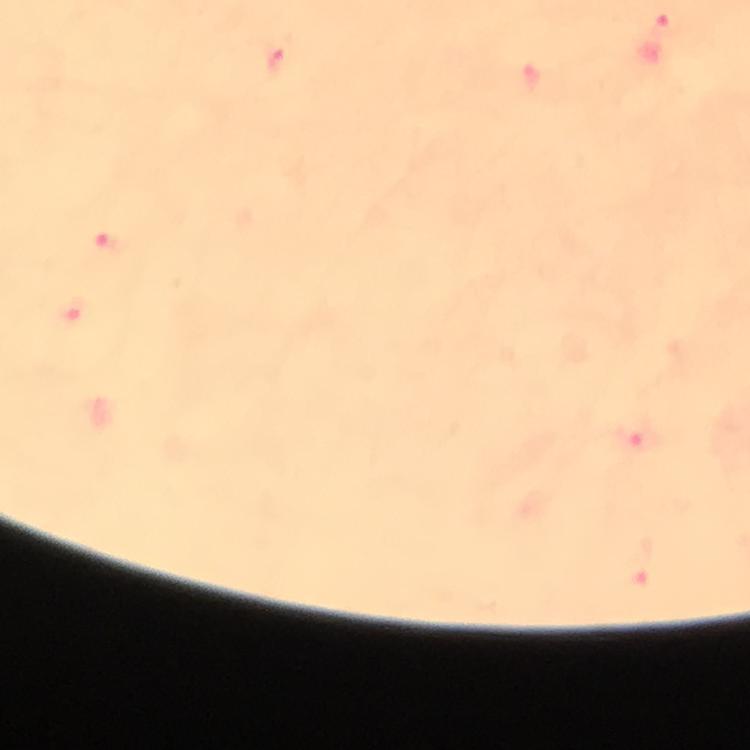

stain = Giemsa
cropped from = a single field of view
image size = 750×750 pixels
context = from a diagnostic examination for malaria
immersion oil = used
preparation = thick blood film
Plasmodium parasite locations = approximate object centers, in pixels from the top-left corner: (x=662, y=22), (x=276, y=63), (x=109, y=242), (x=638, y=439)
capture = smartphone photograph through a microscope
magnification = 100x